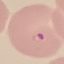

Summary:
  - Malaria status: parasitized
  - Preparation: thin blood smear
  - Image type: cell patch, automatically extracted from a larger field of view and resized to 64 × 64 pixels
  - Stain: Giemsa
  - Capture: smartphone camera at the microscope eyepiece